Assess this cell for malaria.
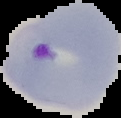
It is parasitized.

image type = cell region segmented out of the field of view; surrounding area masked to black
preparation = thin blood smear
image size = 121×118 pixels